Comment on the morphology of the erythrocytes.
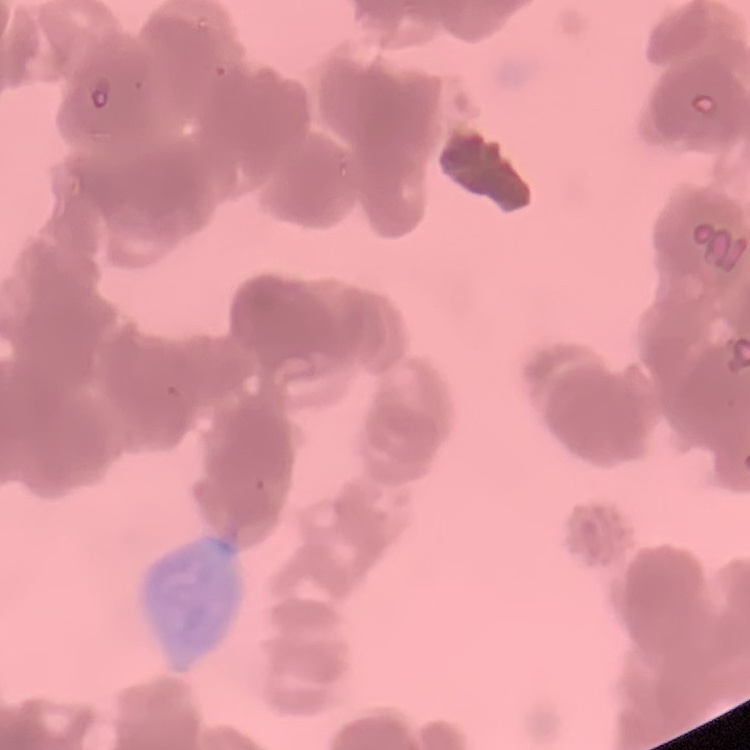

They show rouleaux formation.

Summary:
  - Preparation: thin peripheral smear
  - Image type: one tile cut from a larger photomicrograph
  - Stain: Field's or Giemsa